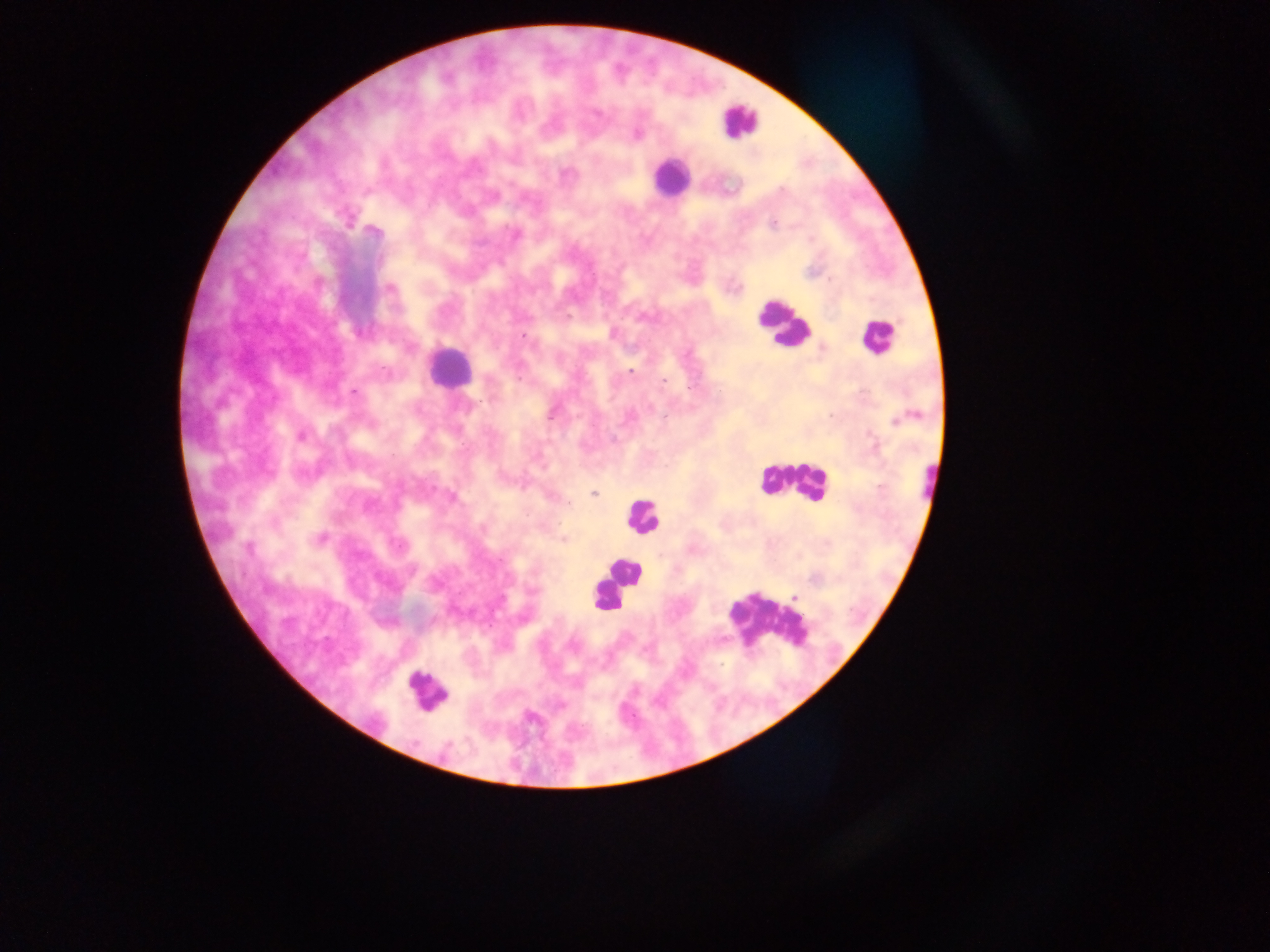

Approximate centers as {x, y} in pixels. Plasmodium parasite locations: {636, 134}, {347, 217}, {772, 222}, {373, 231}, {515, 234}, {612, 333}, {524, 338}, {630, 371}, {353, 393}, {301, 436}, {613, 439}, {593, 494}, {451, 497}, {563, 538}, {319, 539}, {794, 597}. Leukocyte locations: {739, 120}, {670, 177}, {782, 323}, {876, 337}, {448, 367}, {793, 478}, {929, 482}, {642, 517}, {614, 584}, {768, 620}, {426, 691}. Thick blood film. Collected in Ghana. Single field of view. Photographed through a microscope with a mobile-phone camera. Image is 1270×952 pixels.